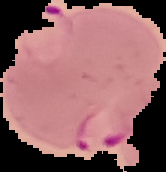
Summary:
  - Image size: 166×172 pixels
  - Image type: segmented cell region with the area outside set to black
  - Malaria status: parasitized
  - Preparation: thin blood smear